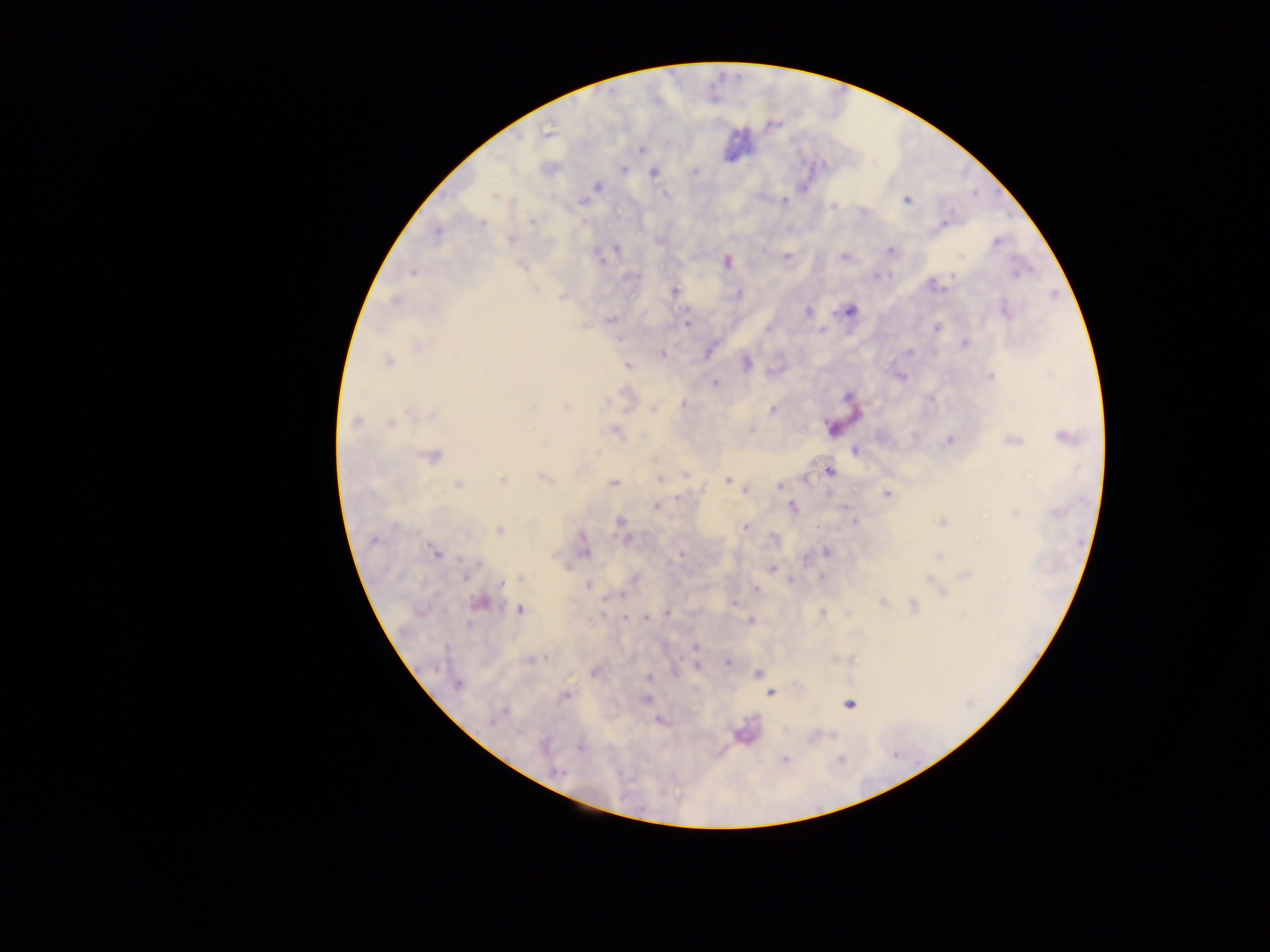

Approximate centers as {x, y} in pixels. Malaria parasite locations: {548, 131}, {641, 148}, {623, 169}, {694, 172}, {653, 173}, {598, 186}, {665, 194}, {493, 197}, {582, 200}, {907, 200}, {783, 201}, {833, 207}, {532, 222}, {583, 222}, {945, 222}, {481, 223}, {437, 232}, {511, 239}, {997, 242}, {616, 249}, {891, 251}, {787, 255}, {963, 256}, {843, 257}, {599, 259}, {726, 262}, {413, 272}, {877, 276}, {629, 277}, {951, 277}, {933, 285}, {674, 291}, {738, 294}, {563, 297}, {396, 301}, {850, 310}, {1005, 310}, {808, 311}, {612, 319}, {686, 322}, {583, 325}, {938, 328}, {768, 329}, {821, 331}, {965, 343}, {419, 348}, {707, 352}, {909, 352}, {661, 354}, {747, 362}, {387, 363}, {627, 365}, {990, 377}, {901, 378}, {715, 383}, {848, 397}, {931, 399}, {610, 403}, {683, 404}, {531, 406}, {565, 406}, {654, 410}, {772, 410}, {409, 414}, {356, 422}, {390, 423}, {832, 428}, {615, 431}, {914, 437}, {1065, 438}, {950, 441}, {1014, 441}, {855, 451}, {596, 454}, {433, 457}, {829, 470}, {684, 475}, {544, 479}, {660, 479}, {804, 479}, {727, 480}, {502, 481}, {458, 484}, {614, 484}, {780, 485}, {746, 491}, {887, 494}, {678, 498}, {656, 507}, {792, 507}, {846, 507}, {1056, 513}, {1014, 514}, {621, 522}, {854, 522}, {942, 523}, {746, 527}, {499, 531}, {583, 537}, {625, 539}, {374, 540}, {434, 552}, {585, 552}, {827, 552}, {681, 554}, {939, 557}, {805, 559}, {478, 564}, {772, 570}, {465, 575}, {967, 575}, {822, 576}, {635, 578}, {520, 579}, {790, 580}, {930, 580}, {503, 583}, {935, 585}, {588, 586}, {757, 590}, {941, 592}, {621, 595}, {481, 602}, {884, 602}, {734, 604}, {913, 606}, {520, 611}, {668, 613}, {822, 615}, {625, 618}, {647, 618}, {751, 621}, {469, 626}, {696, 647}, {531, 660}, {727, 663}, {698, 667}, {674, 670}, {594, 671}, {758, 673}, {648, 678}, {458, 684}, {770, 693}, {565, 696}, {646, 699}, {848, 704}, {505, 711}, {499, 715}, {493, 720}, {662, 722}, {543, 746}, {579, 747}, {785, 760}, {556, 771}. Image is 1270×952 pixels. Thick blood film. Single field of view. Collected in Ghana. Mobile-phone photograph taken through the microscope.